Locate every blood parasite and identify its species.
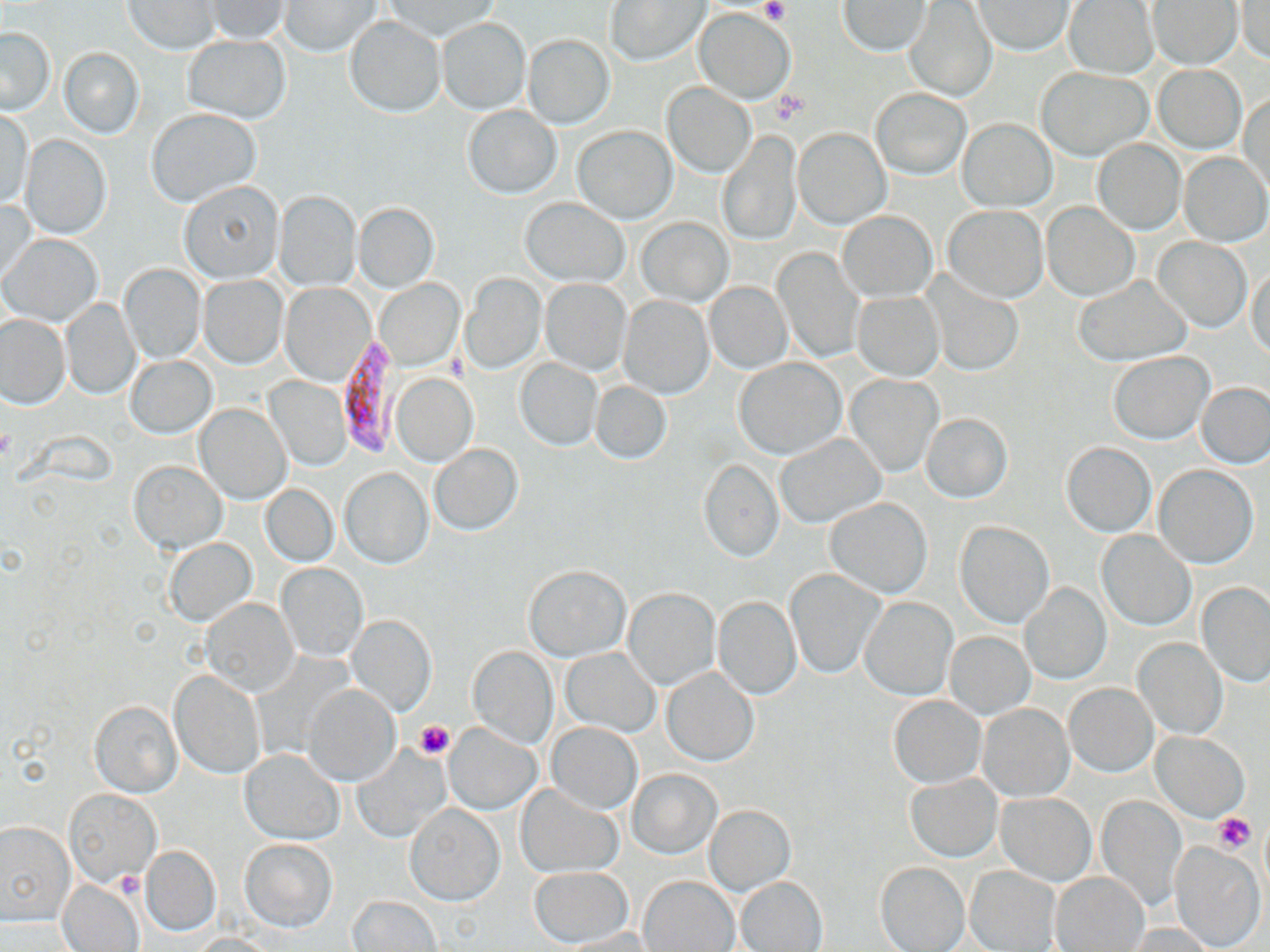
Approximate bounding boxes as (x1,y1)-(x2,y2) corner pairs in pixels.
Plasmodium falciparum-infected red blood cells: (334,340)-(400,457).
No Plasmodium ovale, Plasmodium malariae, Plasmodium vivax, Babesia divergens, or Trypanosoma brucei observed.

Uninfected red blood cell locations: (203,0)-(291,43), (606,0)-(710,65), (124,1)-(222,55), (281,1)-(379,56), (383,1)-(499,41), (905,1)-(997,102), (971,1)-(1074,55), (1063,1)-(1158,79), (1149,1)-(1242,68), (839,2)-(930,56), (1236,3)-(1270,64), (694,8)-(793,103), (344,17)-(445,117), (436,17)-(531,115), (0,27)-(55,114), (184,35)-(291,123), (522,35)-(615,128), (59,48)-(143,138), (1153,66)-(1246,152), (1038,67)-(1152,159), (662,83)-(755,177), (871,87)-(970,180), (1239,92)-(1269,191), (462,106)-(562,198), (2,109)-(33,208), (147,109)-(261,206), (959,118)-(1056,211), (573,125)-(677,224), (794,127)-(890,228), (717,129)-(801,246), (21,135)-(112,238), (1092,141)-(1184,235), (1179,152)-(1269,247), (177,179)-(283,284), (274,191)-(361,291), (1,199)-(38,282), (522,199)-(629,286), (355,202)-(439,292), (1042,203)-(1137,300), (943,206)-(1047,301), (837,210)-(937,302), (637,216)-(733,307), (1,233)-(103,327), (1152,237)-(1251,333), (772,247)-(864,364), (1246,264)-(1270,358), (120,265)-(206,363), (460,274)-(545,373), (200,276)-(287,368), (1073,276)-(1193,364), (925,277)-(1022,377), (540,278)-(632,375), (377,280)-(463,366), (705,281)-(791,373), (280,283)-(375,386), (852,291)-(944,380), (618,294)-(714,399), (61,300)-(141,398), (1,314)-(69,407), (1109,352)-(1212,443), (126,356)-(216,438), (517,358)-(602,451), (734,359)-(844,458), (391,373)-(478,467), (846,375)-(942,476), (265,377)-(350,470), (591,381)-(671,464), (1198,382)-(1270,468), (196,404)-(290,504), (923,414)-(1012,502), (775,434)-(886,528), (1061,442)-(1155,536), (430,444)-(523,535), (700,459)-(782,561), (130,461)-(227,553), (1155,466)-(1257,568), (339,467)-(433,569), (262,484)-(337,566), (825,498)-(932,598), (956,521)-(1054,627), (1097,530)-(1195,630), (164,537)-(257,625), (276,563)-(366,661), (523,564)-(631,662), (787,570)-(882,678), (1196,581)-(1270,686), (1021,583)-(1111,684), (625,588)-(718,689), (712,595)-(801,699), (861,596)-(957,700), (201,599)-(297,695), (348,614)-(437,717), (946,631)-(1034,718), (1134,639)-(1226,739), (468,645)-(558,748), (562,648)-(659,736), (662,667)-(758,764), (169,669)-(265,778), (1064,683)-(1158,776), (306,685)-(401,786), (889,695)-(985,787), (89,700)-(181,797), (979,703)-(1073,800), (445,723)-(542,814), (547,723)-(641,814), (1152,733)-(1249,821), (351,746)-(450,842), (240,749)-(344,844), (629,769)-(721,858), (906,773)-(1002,861), (515,784)-(622,877), (65,789)-(160,887), (997,793)-(1095,885), (1098,795)-(1188,909), (405,804)-(504,905), (706,804)-(795,894), (0,821)-(74,925), (240,838)-(338,932), (1170,842)-(1264,951), (141,846)-(220,936), (875,861)-(969,952), (964,865)-(1060,952), (528,867)-(633,947), (1052,872)-(1150,951), (737,876)-(828,952), (58,877)-(143,952), (640,877)-(738,952), (350,895)-(442,951), (1125,923)-(1217,951), (554,929)-(657,951), (190,934)-(279,951). Platelet locations: (761,1)-(787,23), (0,429)-(14,462), (414,720)-(454,759), (1212,813)-(1256,852), (113,872)-(145,899). Slide-level diagnosis: Plasmodium falciparum. May-Grünwald-Giemsa-stained preparation. Image is 1270×952 pixels. Captured at 1000x magnification. One field of a larger specimen. Light microscopy. Thin blood film.